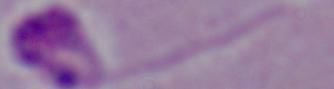
modality = micrograph
identification = Leishmania
magnification = 1000x